Name the blood parasite species.
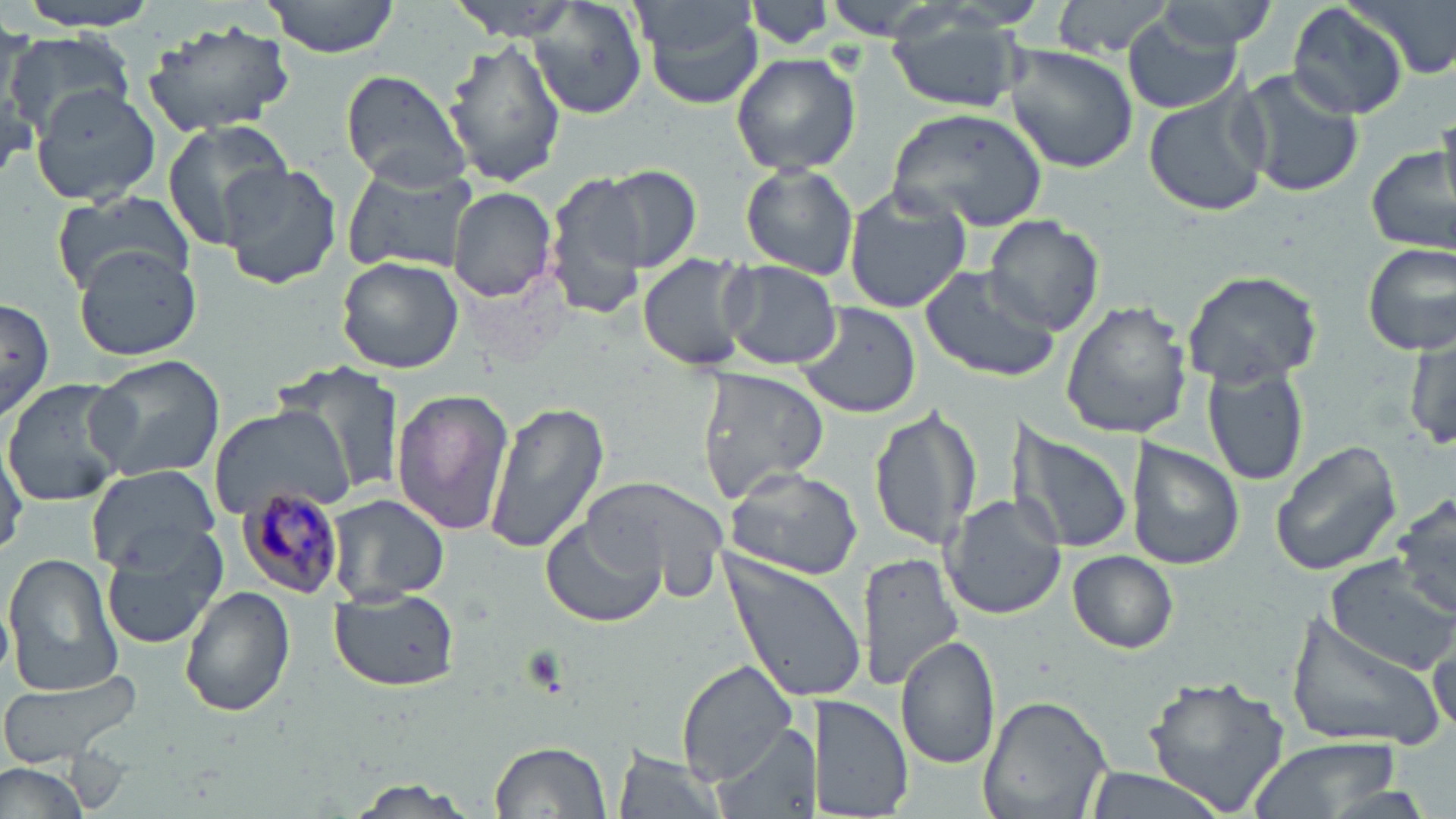
Plasmodium malariae.

uninfected red blood cell locations = approximate bounding boxes as named x1/y1/x2/y2 corners in pixels: (x1=13, y1=0, x2=161, y2=32), (x1=260, y1=0, x2=405, y2=59), (x1=452, y1=0, x2=587, y2=39), (x1=631, y1=0, x2=768, y2=110), (x1=744, y1=0, x2=838, y2=52), (x1=812, y1=0, x2=972, y2=35), (x1=1141, y1=0, x2=1280, y2=57), (x1=1349, y1=0, x2=1454, y2=82), (x1=531, y1=1, x2=648, y2=119), (x1=1051, y1=1, x2=1177, y2=58), (x1=1285, y1=1, x2=1417, y2=119), (x1=1122, y1=7, x2=1248, y2=115), (x1=885, y1=17, x2=1026, y2=115), (x1=139, y1=18, x2=297, y2=139), (x1=2, y1=33, x2=135, y2=139), (x1=441, y1=36, x2=567, y2=189), (x1=1002, y1=41, x2=1137, y2=174), (x1=730, y1=52, x2=861, y2=176), (x1=1235, y1=66, x2=1363, y2=198), (x1=339, y1=71, x2=472, y2=191), (x1=29, y1=83, x2=161, y2=207), (x1=1142, y1=86, x2=1272, y2=219), (x1=886, y1=107, x2=1046, y2=226), (x1=1437, y1=111, x2=1456, y2=217), (x1=160, y1=117, x2=296, y2=251), (x1=1366, y1=135, x2=1454, y2=257), (x1=339, y1=160, x2=480, y2=275), (x1=220, y1=162, x2=341, y2=291), (x1=739, y1=164, x2=858, y2=279), (x1=593, y1=165, x2=702, y2=273), (x1=546, y1=169, x2=654, y2=319), (x1=842, y1=184, x2=973, y2=313), (x1=447, y1=186, x2=558, y2=301), (x1=50, y1=189, x2=195, y2=295), (x1=985, y1=214, x2=1104, y2=333), (x1=1361, y1=240, x2=1456, y2=354), (x1=74, y1=246, x2=203, y2=363), (x1=637, y1=252, x2=757, y2=374), (x1=335, y1=255, x2=464, y2=374), (x1=717, y1=258, x2=843, y2=370), (x1=919, y1=264, x2=1064, y2=383), (x1=1180, y1=269, x2=1324, y2=387), (x1=1, y1=297, x2=56, y2=423), (x1=1060, y1=300, x2=1191, y2=440), (x1=793, y1=301, x2=922, y2=420), (x1=1405, y1=327, x2=1455, y2=455), (x1=87, y1=354, x2=226, y2=482), (x1=279, y1=360, x2=412, y2=503), (x1=1203, y1=366, x2=1308, y2=488), (x1=695, y1=367, x2=828, y2=504), (x1=2, y1=378, x2=131, y2=506), (x1=390, y1=389, x2=513, y2=538), (x1=481, y1=399, x2=609, y2=556), (x1=868, y1=403, x2=983, y2=553), (x1=206, y1=405, x2=354, y2=518), (x1=1008, y1=421, x2=1137, y2=559), (x1=1, y1=435, x2=28, y2=556), (x1=1128, y1=438, x2=1246, y2=572), (x1=1270, y1=439, x2=1404, y2=577), (x1=720, y1=463, x2=865, y2=580), (x1=83, y1=465, x2=219, y2=573), (x1=584, y1=473, x2=733, y2=596), (x1=1391, y1=490, x2=1456, y2=622), (x1=940, y1=493, x2=1064, y2=619), (x1=326, y1=494, x2=450, y2=604), (x1=540, y1=518, x2=667, y2=629), (x1=100, y1=532, x2=224, y2=649), (x1=719, y1=549, x2=865, y2=704), (x1=1068, y1=550, x2=1178, y2=653), (x1=859, y1=551, x2=965, y2=697), (x1=3, y1=552, x2=123, y2=696), (x1=1325, y1=555, x2=1456, y2=675), (x1=180, y1=587, x2=296, y2=719), (x1=329, y1=589, x2=459, y2=692), (x1=1282, y1=606, x2=1450, y2=755), (x1=896, y1=636, x2=1001, y2=769), (x1=1429, y1=638, x2=1453, y2=735), (x1=677, y1=661, x2=802, y2=784), (x1=0, y1=666, x2=148, y2=766), (x1=1143, y1=677, x2=1290, y2=812), (x1=815, y1=692, x2=915, y2=819), (x1=979, y1=693, x2=1112, y2=818), (x1=711, y1=723, x2=818, y2=819), (x1=1245, y1=735, x2=1403, y2=817), (x1=488, y1=739, x2=613, y2=819), (x1=611, y1=745, x2=728, y2=819), (x1=0, y1=760, x2=92, y2=819), (x1=1081, y1=766, x2=1231, y2=819), (x1=342, y1=775, x2=487, y2=818)
Plasmodium malariae-infected red blood cell locations = approximate bounding boxes as named x1/y1/x2/y2 corners in pixels: (x1=238, y1=485, x2=343, y2=599)
stain = May-Grünwald-Giemsa
magnification = 1000x
modality = light microscopy
preparation = thin blood smear
field of view = one of a larger specimen
image size = 1456×819 pixels